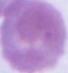

Summary:
  - Modality: micrograph
  - Identification: erythrocyte
  - Magnification: 1000x